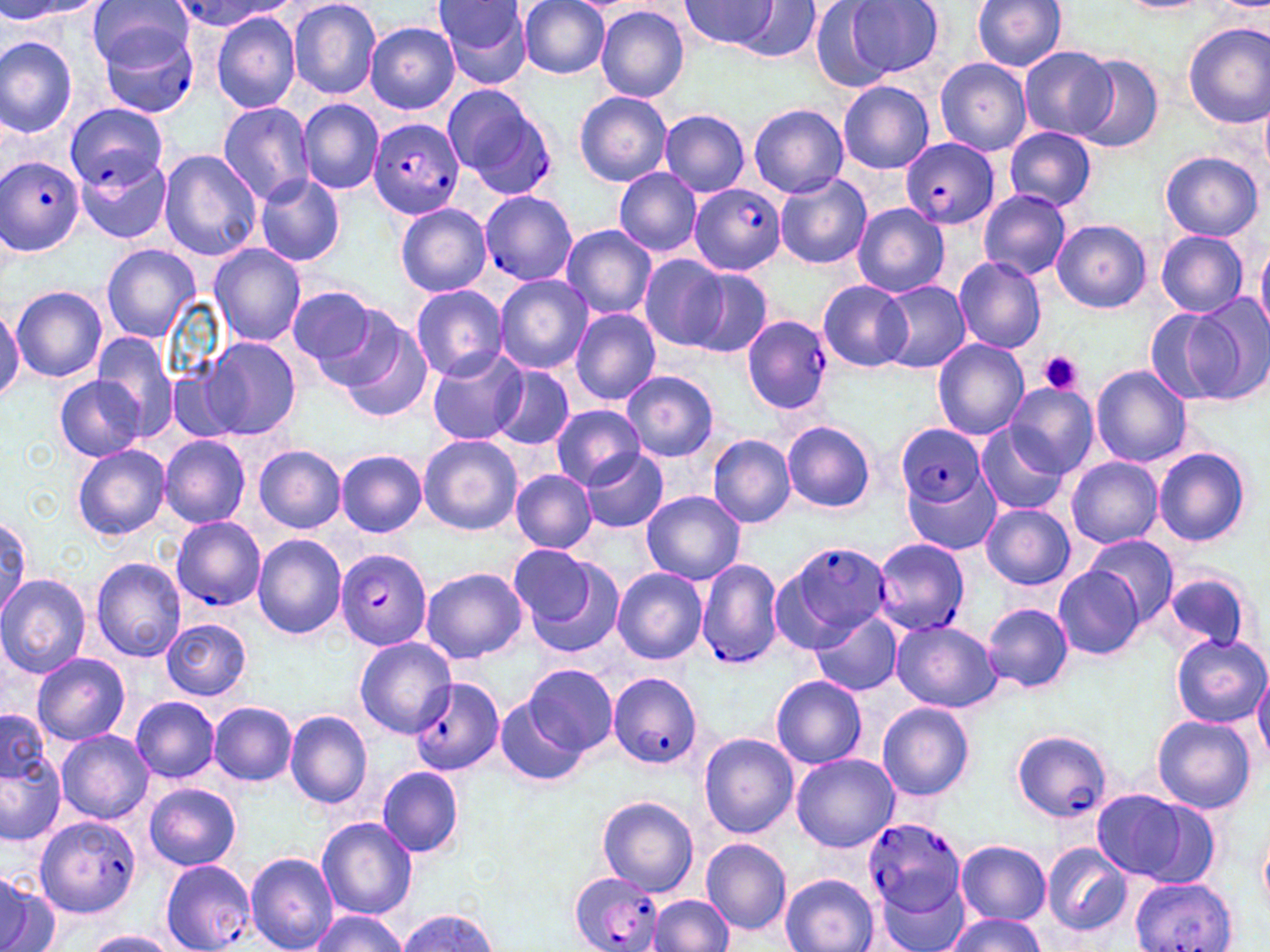

slide-level diagnosis = Plasmodium falciparum
modality = optical microscopy
field of view = single
preparation = thin blood smear
magnification = 1000x
uninfected red blood cell locations = approximate bounding boxes as named x1/y1/x2/y2 corners in pixels: (x1=89, y1=0, x2=192, y2=76), (x1=431, y1=0, x2=534, y2=87), (x1=518, y1=0, x2=612, y2=79), (x1=681, y1=0, x2=776, y2=51), (x1=845, y1=0, x2=944, y2=77), (x1=972, y1=0, x2=1067, y2=72), (x1=1217, y1=0, x2=1270, y2=9), (x1=0, y1=1, x2=108, y2=21), (x1=289, y1=1, x2=381, y2=99), (x1=734, y1=1, x2=821, y2=64), (x1=809, y1=1, x2=895, y2=93), (x1=1120, y1=1, x2=1211, y2=14), (x1=595, y1=5, x2=690, y2=104), (x1=212, y1=12, x2=302, y2=113), (x1=1183, y1=22, x2=1269, y2=129), (x1=365, y1=23, x2=460, y2=114), (x1=0, y1=35, x2=79, y2=136), (x1=1020, y1=49, x2=1116, y2=139), (x1=1073, y1=53, x2=1165, y2=154), (x1=935, y1=58, x2=1032, y2=155), (x1=837, y1=80, x2=935, y2=175), (x1=575, y1=91, x2=672, y2=186), (x1=297, y1=100, x2=384, y2=194), (x1=216, y1=101, x2=316, y2=205), (x1=1260, y1=101, x2=1270, y2=178), (x1=66, y1=102, x2=167, y2=190), (x1=749, y1=102, x2=848, y2=199), (x1=658, y1=109, x2=750, y2=198), (x1=1005, y1=127, x2=1097, y2=211), (x1=158, y1=149, x2=262, y2=262), (x1=1160, y1=151, x2=1263, y2=243), (x1=612, y1=167, x2=703, y2=258), (x1=774, y1=174, x2=873, y2=270), (x1=254, y1=175, x2=345, y2=267), (x1=979, y1=191, x2=1072, y2=278), (x1=962, y1=196, x2=1079, y2=348), (x1=395, y1=203, x2=491, y2=295), (x1=851, y1=204, x2=949, y2=296), (x1=1053, y1=220, x2=1151, y2=312), (x1=560, y1=224, x2=657, y2=322), (x1=1156, y1=231, x2=1248, y2=317), (x1=1256, y1=243, x2=1270, y2=336), (x1=101, y1=244, x2=200, y2=341), (x1=210, y1=244, x2=307, y2=345), (x1=639, y1=255, x2=732, y2=351), (x1=953, y1=256, x2=1047, y2=354), (x1=685, y1=268, x2=773, y2=358), (x1=494, y1=275, x2=593, y2=372), (x1=818, y1=280, x2=910, y2=372), (x1=878, y1=282, x2=971, y2=373), (x1=410, y1=284, x2=509, y2=381), (x1=11, y1=286, x2=107, y2=381), (x1=289, y1=287, x2=387, y2=381), (x1=1190, y1=297, x2=1269, y2=403), (x1=0, y1=306, x2=22, y2=401), (x1=569, y1=308, x2=661, y2=405), (x1=1149, y1=308, x2=1243, y2=404), (x1=336, y1=317, x2=435, y2=423), (x1=89, y1=332, x2=181, y2=438), (x1=200, y1=338, x2=302, y2=441), (x1=932, y1=338, x2=1029, y2=441), (x1=426, y1=349, x2=527, y2=445), (x1=488, y1=365, x2=574, y2=451), (x1=1090, y1=365, x2=1192, y2=467), (x1=168, y1=369, x2=240, y2=443), (x1=621, y1=370, x2=720, y2=463), (x1=54, y1=375, x2=145, y2=462), (x1=1005, y1=382, x2=1098, y2=477), (x1=550, y1=406, x2=646, y2=488), (x1=782, y1=420, x2=876, y2=514), (x1=975, y1=423, x2=1072, y2=517), (x1=418, y1=434, x2=522, y2=535), (x1=707, y1=434, x2=796, y2=529), (x1=158, y1=435, x2=250, y2=528), (x1=72, y1=444, x2=170, y2=540), (x1=254, y1=445, x2=346, y2=531), (x1=580, y1=447, x2=669, y2=532), (x1=1153, y1=447, x2=1251, y2=547), (x1=337, y1=450, x2=426, y2=537), (x1=1067, y1=457, x2=1163, y2=548), (x1=510, y1=470, x2=597, y2=553), (x1=906, y1=472, x2=1002, y2=554), (x1=641, y1=490, x2=745, y2=585), (x1=981, y1=502, x2=1075, y2=590), (x1=0, y1=514, x2=29, y2=616), (x1=253, y1=535, x2=347, y2=640), (x1=1085, y1=536, x2=1178, y2=621), (x1=514, y1=546, x2=626, y2=656), (x1=90, y1=557, x2=187, y2=663), (x1=421, y1=566, x2=528, y2=662), (x1=1054, y1=566, x2=1145, y2=660), (x1=612, y1=568, x2=708, y2=664), (x1=1164, y1=572, x2=1253, y2=650), (x1=0, y1=574, x2=90, y2=676), (x1=983, y1=602, x2=1073, y2=692), (x1=810, y1=611, x2=901, y2=697), (x1=161, y1=618, x2=251, y2=700), (x1=890, y1=620, x2=1000, y2=711), (x1=1172, y1=634, x2=1268, y2=726), (x1=354, y1=637, x2=454, y2=737), (x1=32, y1=654, x2=130, y2=745), (x1=524, y1=663, x2=619, y2=755), (x1=1254, y1=667, x2=1270, y2=763), (x1=771, y1=676, x2=867, y2=768), (x1=131, y1=696, x2=219, y2=782), (x1=494, y1=696, x2=586, y2=787), (x1=209, y1=701, x2=297, y2=785), (x1=879, y1=703, x2=974, y2=801), (x1=1, y1=709, x2=51, y2=788), (x1=284, y1=711, x2=372, y2=808), (x1=1150, y1=713, x2=1257, y2=815), (x1=55, y1=729, x2=153, y2=824), (x1=700, y1=733, x2=799, y2=838), (x1=0, y1=749, x2=66, y2=845), (x1=791, y1=754, x2=899, y2=852), (x1=376, y1=766, x2=464, y2=859), (x1=144, y1=783, x2=242, y2=870), (x1=1089, y1=789, x2=1204, y2=883), (x1=596, y1=795, x2=699, y2=895), (x1=317, y1=817, x2=417, y2=919), (x1=1257, y1=824, x2=1270, y2=917), (x1=700, y1=838, x2=791, y2=936), (x1=954, y1=840, x2=1051, y2=925), (x1=1042, y1=842, x2=1133, y2=937), (x1=245, y1=849, x2=338, y2=952), (x1=0, y1=872, x2=58, y2=952), (x1=779, y1=872, x2=879, y2=952), (x1=878, y1=886, x2=970, y2=951), (x1=649, y1=894, x2=734, y2=952), (x1=396, y1=909, x2=499, y2=951), (x1=308, y1=912, x2=409, y2=952), (x1=943, y1=914, x2=1046, y2=952), (x1=83, y1=931, x2=181, y2=952)
image size = 1270×952 pixels
stain = May-Grünwald-Giemsa
Plasmodium falciparum-infected red blood cell locations = approximate bounding boxes as named x1/y1/x2/y2 corners in pixels: (x1=168, y1=1, x2=289, y2=32), (x1=99, y1=22, x2=201, y2=118), (x1=446, y1=87, x2=555, y2=199), (x1=369, y1=117, x2=465, y2=218), (x1=900, y1=137, x2=1000, y2=229), (x1=0, y1=152, x2=83, y2=257), (x1=75, y1=155, x2=170, y2=245), (x1=690, y1=184, x2=786, y2=274), (x1=478, y1=189, x2=576, y2=286), (x1=742, y1=314, x2=833, y2=414), (x1=898, y1=425, x2=984, y2=505), (x1=170, y1=517, x2=264, y2=610), (x1=872, y1=536, x2=969, y2=637), (x1=776, y1=540, x2=893, y2=650), (x1=335, y1=546, x2=432, y2=651), (x1=695, y1=559, x2=783, y2=670), (x1=608, y1=671, x2=703, y2=770), (x1=409, y1=674, x2=505, y2=775), (x1=1009, y1=727, x2=1111, y2=821), (x1=35, y1=816, x2=139, y2=916), (x1=864, y1=818, x2=967, y2=919), (x1=158, y1=859, x2=254, y2=952), (x1=569, y1=872, x2=667, y2=952), (x1=1128, y1=876, x2=1238, y2=952)
platelet locations = approximate bounding boxes as named x1/y1/x2/y2 corners in pixels: (x1=1039, y1=350, x2=1082, y2=395)